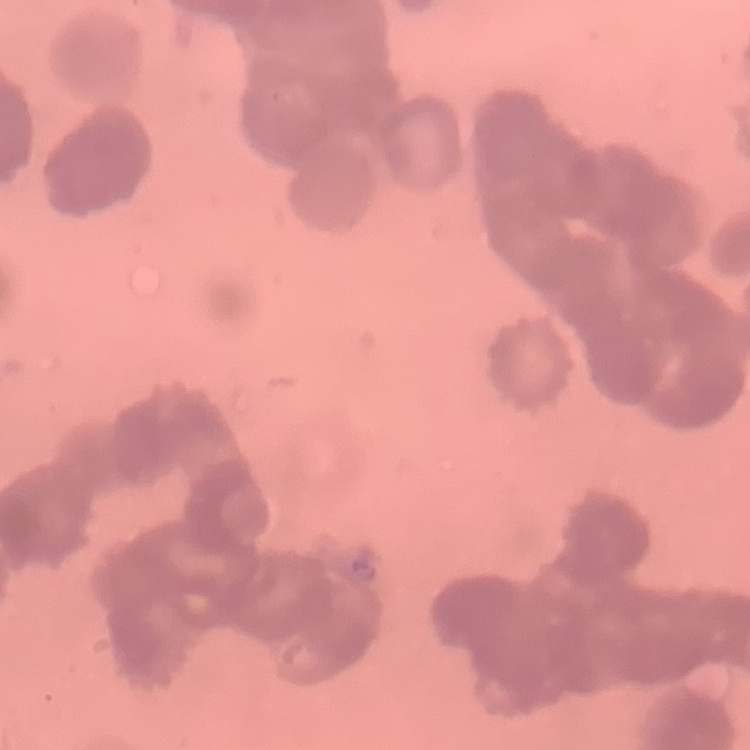

The erythrocytes show rouleaux formation. Stained with either Field's or Giemsa. Thin blood smear. Square crop of a larger photomicrograph.